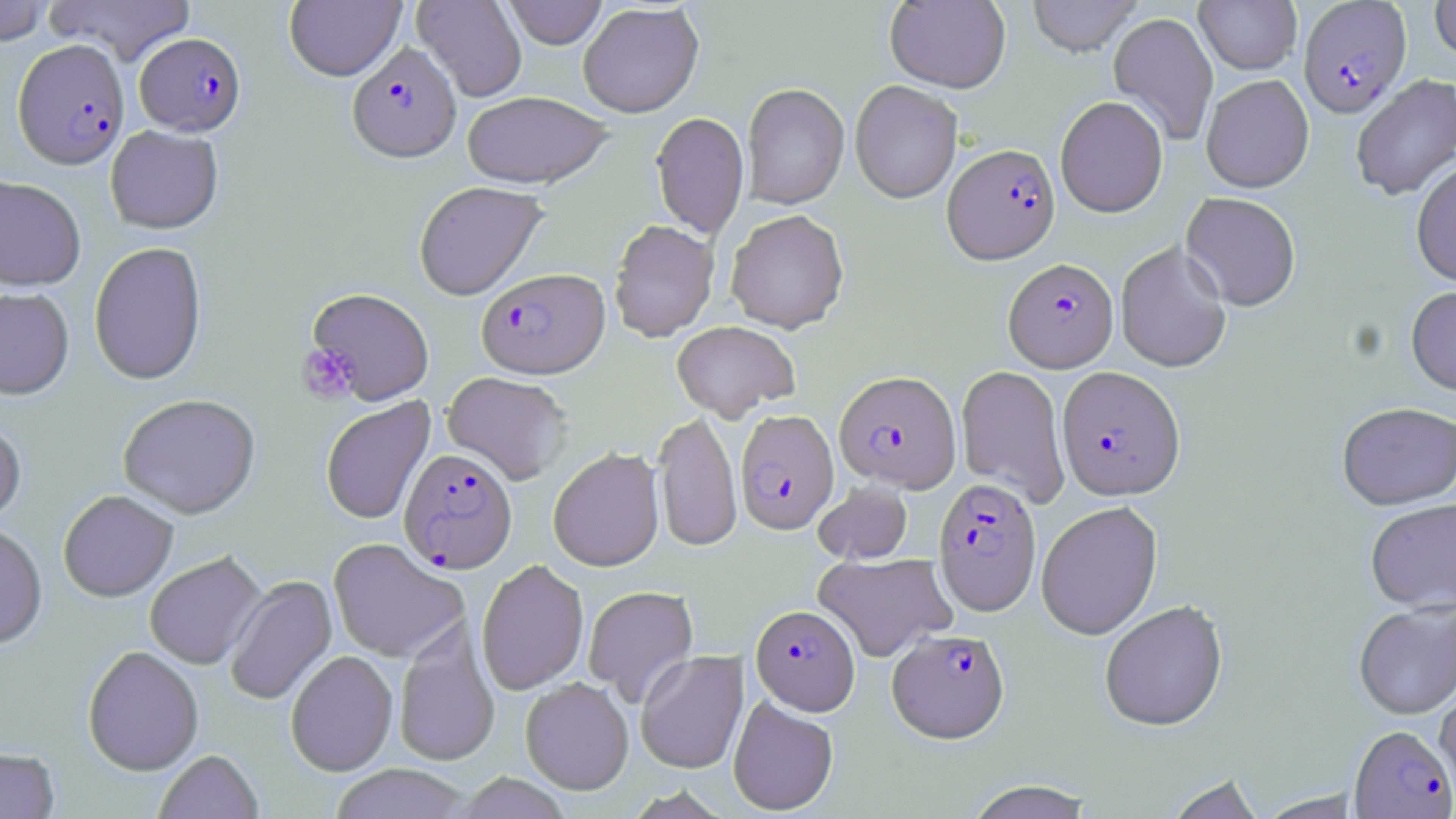

slide-level diagnosis = Plasmodium falciparum
magnification = 1000x
preparation = thin blood film
stain = May-Grünwald-Giemsa
Plasmodium falciparum-infected red blood cell locations = approximate bounding boxes as named x1/y1/x2/y2 corners in pixels: (x1=1298, y1=0, x2=1412, y2=118), (x1=135, y1=32, x2=246, y2=136), (x1=12, y1=39, x2=129, y2=170), (x1=347, y1=42, x2=462, y2=165), (x1=943, y1=143, x2=1060, y2=265), (x1=1004, y1=258, x2=1119, y2=373), (x1=476, y1=269, x2=610, y2=380), (x1=1056, y1=367, x2=1185, y2=501), (x1=834, y1=370, x2=961, y2=493), (x1=734, y1=409, x2=839, y2=535), (x1=399, y1=448, x2=518, y2=575), (x1=933, y1=478, x2=1042, y2=617), (x1=751, y1=604, x2=859, y2=715), (x1=888, y1=628, x2=1010, y2=743), (x1=1350, y1=726, x2=1455, y2=818)
platelet locations = approximate bounding boxes as named x1/y1/x2/y2 corners in pixels: (x1=296, y1=343, x2=361, y2=405)
image size = 1456×819 pixels
uninfected red blood cell locations = approximate bounding boxes as named x1/y1/x2/y2 corners in pixels: (x1=43, y1=0, x2=197, y2=65), (x1=284, y1=0, x2=406, y2=82), (x1=411, y1=0, x2=528, y2=103), (x1=501, y1=0, x2=608, y2=50), (x1=885, y1=0, x2=1011, y2=93), (x1=1026, y1=0, x2=1143, y2=57), (x1=1194, y1=0, x2=1302, y2=75), (x1=1429, y1=0, x2=1456, y2=62), (x1=0, y1=1, x2=55, y2=46), (x1=578, y1=3, x2=704, y2=119), (x1=1108, y1=12, x2=1219, y2=147), (x1=1201, y1=74, x2=1314, y2=193), (x1=1350, y1=74, x2=1456, y2=201), (x1=849, y1=80, x2=963, y2=204), (x1=742, y1=83, x2=849, y2=210), (x1=462, y1=91, x2=613, y2=191), (x1=1055, y1=96, x2=1168, y2=218), (x1=650, y1=113, x2=749, y2=240), (x1=105, y1=126, x2=224, y2=235), (x1=1411, y1=160, x2=1456, y2=288), (x1=0, y1=177, x2=86, y2=291), (x1=413, y1=182, x2=548, y2=302), (x1=1180, y1=192, x2=1301, y2=312), (x1=725, y1=209, x2=850, y2=334), (x1=609, y1=221, x2=720, y2=343), (x1=1115, y1=241, x2=1232, y2=372), (x1=89, y1=242, x2=208, y2=387), (x1=1406, y1=286, x2=1456, y2=397), (x1=0, y1=288, x2=74, y2=400), (x1=307, y1=289, x2=435, y2=405), (x1=672, y1=321, x2=800, y2=421), (x1=955, y1=365, x2=1070, y2=507), (x1=441, y1=372, x2=572, y2=485), (x1=118, y1=394, x2=261, y2=520), (x1=320, y1=397, x2=436, y2=526), (x1=1337, y1=403, x2=1455, y2=511), (x1=654, y1=411, x2=742, y2=553), (x1=0, y1=419, x2=26, y2=529), (x1=548, y1=447, x2=665, y2=572), (x1=813, y1=482, x2=912, y2=565), (x1=58, y1=491, x2=179, y2=603), (x1=1365, y1=498, x2=1456, y2=613), (x1=1036, y1=500, x2=1163, y2=640), (x1=0, y1=525, x2=47, y2=650), (x1=328, y1=538, x2=469, y2=663), (x1=144, y1=552, x2=267, y2=670), (x1=813, y1=552, x2=957, y2=662), (x1=476, y1=560, x2=589, y2=696), (x1=224, y1=575, x2=338, y2=707), (x1=583, y1=585, x2=699, y2=707), (x1=1099, y1=599, x2=1228, y2=733), (x1=1353, y1=600, x2=1456, y2=719), (x1=393, y1=617, x2=501, y2=768), (x1=82, y1=646, x2=204, y2=776), (x1=285, y1=650, x2=398, y2=777), (x1=635, y1=650, x2=749, y2=774), (x1=520, y1=678, x2=633, y2=795), (x1=1435, y1=685, x2=1456, y2=803), (x1=728, y1=697, x2=839, y2=815), (x1=0, y1=747, x2=60, y2=818), (x1=154, y1=750, x2=263, y2=819), (x1=328, y1=765, x2=473, y2=818), (x1=453, y1=773, x2=574, y2=819), (x1=964, y1=780, x2=1099, y2=819)
field of view = single
modality = optical microscopy